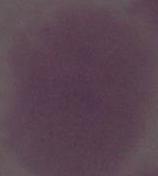
Summary:
  - Identification: red blood cell
  - Magnification: 1000x
  - Modality: photomicrograph